Identify the parasite.
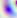
This is Toxoplasma gondii.

Captured at 400x magnification. Photomicrograph.